Comment on the morphology of the red blood cells.
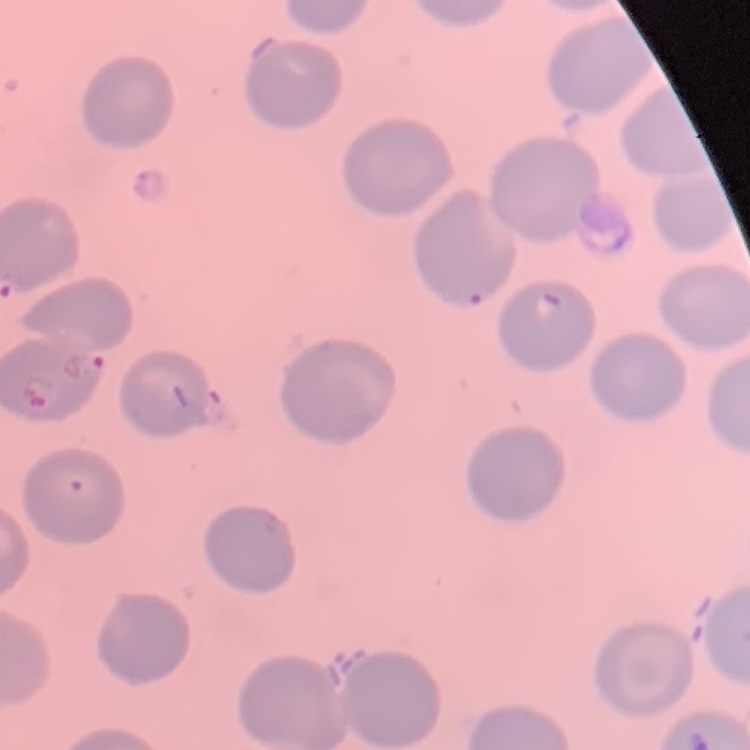
No rouleaux formation.

Thin blood film. Square crop of a larger photomicrograph. Stained with either Field's or Giemsa.